Assess this cell for malaria.
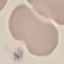

It is uninfected.

Summary:
  - Image type: cell patch, automatically extracted from a larger field of view and resized to 64 × 64 pixels
  - Capture: smartphone camera at the microscope eyepiece
  - Stain: Giemsa
  - Preparation: thin blood film